Assess this cell for malaria.
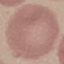
Uninfected.

Acquired by smartphone through the microscope eyepiece. Giemsa stain. Cell patch, automatically extracted from a larger field of view and resized to 64 × 64 pixels. Thin blood film.